Classify this cell by malaria status.
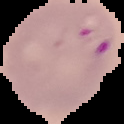
It is parasitized.

Segmented cell region on a black background. Image is 124×124 pixels. From a thin blood film.